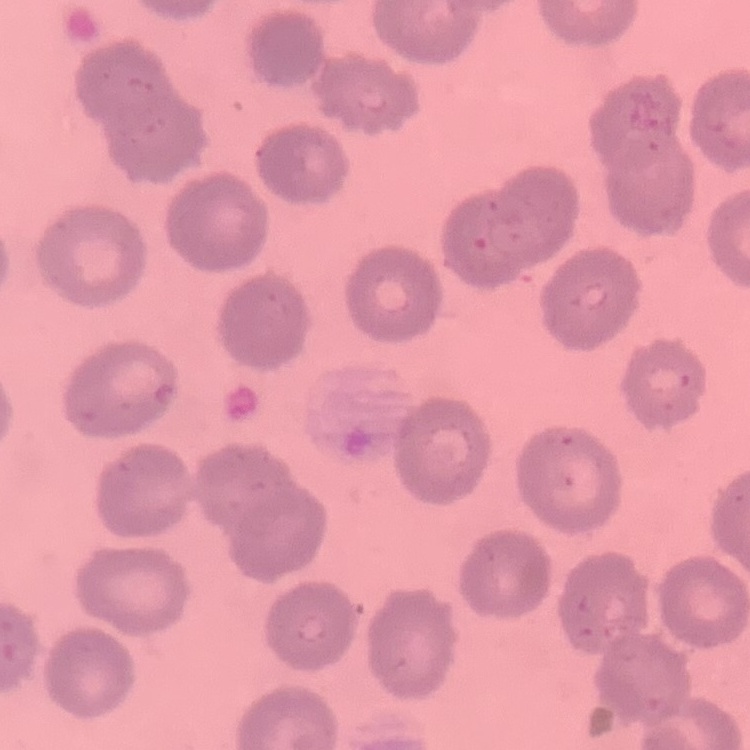

Summary:
  - Red blood cell morphology: no rouleaux formation
  - Preparation: thin peripheral smear
  - Stain: Field's or Giemsa
  - Image type: one tile cut from a larger photomicrograph